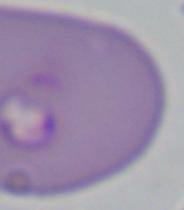
identification = Babesia
modality = micrograph
magnification = 1000x